Give the extent of all Plasmodium vivax-infected red blood cells.
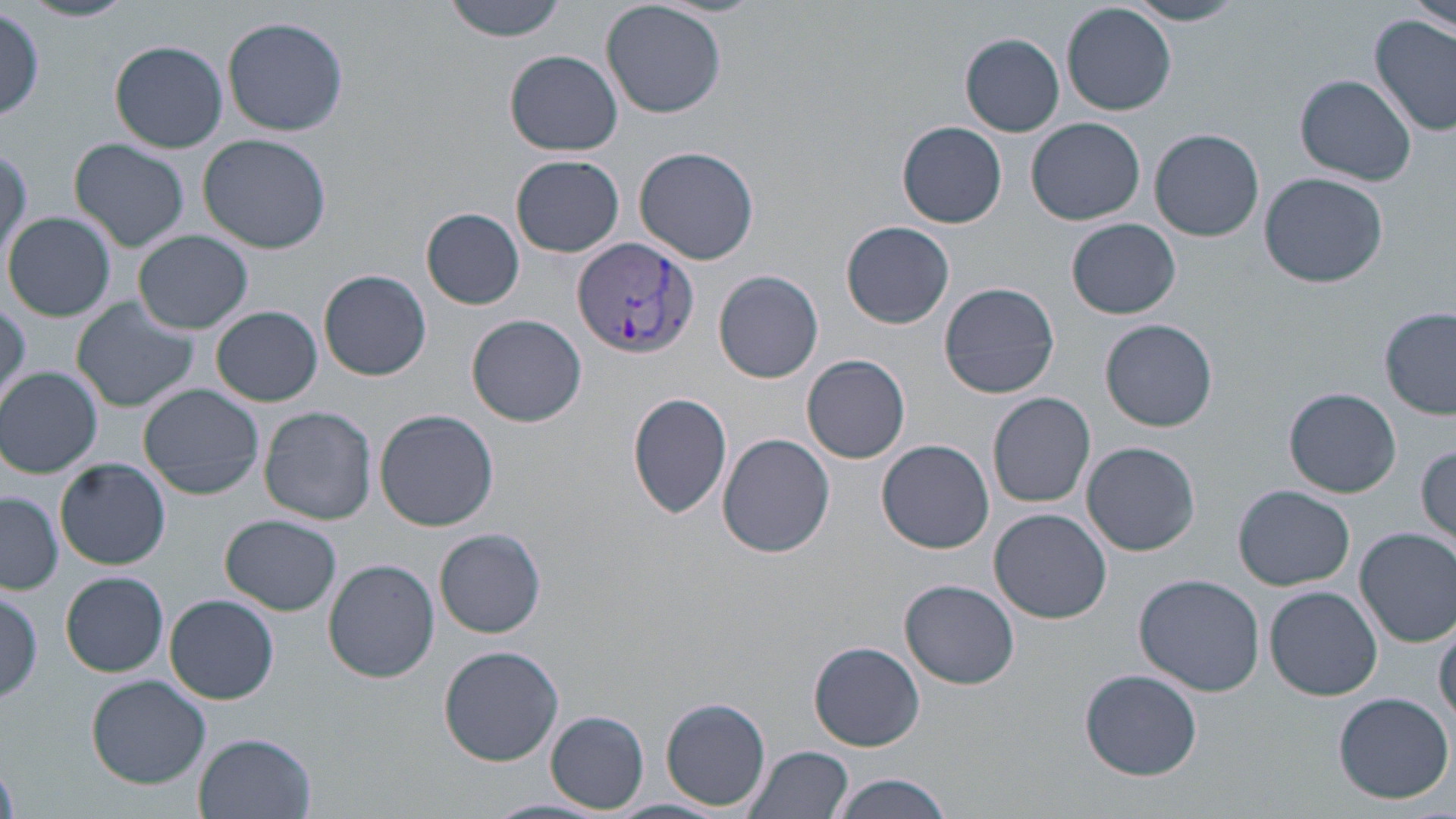

Approximate bounding boxes as named x1/y1/x2/y2 corners in pixels.
Plasmodium vivax-infected red blood cells: (x1=572, y1=236, x2=697, y2=359).

Uninfected red blood cell locations: (x1=23, y1=0, x2=136, y2=23), (x1=442, y1=0, x2=568, y2=42), (x1=603, y1=0, x2=729, y2=119), (x1=1410, y1=0, x2=1454, y2=35), (x1=1125, y1=1, x2=1247, y2=26), (x1=1062, y1=3, x2=1176, y2=115), (x1=1, y1=9, x2=46, y2=121), (x1=222, y1=16, x2=349, y2=136), (x1=1371, y1=17, x2=1456, y2=137), (x1=961, y1=34, x2=1063, y2=136), (x1=111, y1=40, x2=227, y2=152), (x1=506, y1=50, x2=622, y2=156), (x1=1294, y1=73, x2=1416, y2=185), (x1=1027, y1=117, x2=1145, y2=225), (x1=897, y1=122, x2=1007, y2=229), (x1=1149, y1=129, x2=1264, y2=242), (x1=197, y1=133, x2=332, y2=253), (x1=70, y1=138, x2=190, y2=252), (x1=635, y1=144, x2=761, y2=265), (x1=512, y1=155, x2=624, y2=257), (x1=1258, y1=172, x2=1388, y2=287), (x1=422, y1=207, x2=524, y2=309), (x1=5, y1=211, x2=115, y2=322), (x1=1068, y1=219, x2=1182, y2=320), (x1=842, y1=221, x2=954, y2=329), (x1=135, y1=230, x2=253, y2=334), (x1=319, y1=269, x2=432, y2=380), (x1=714, y1=270, x2=824, y2=383), (x1=939, y1=281, x2=1059, y2=398), (x1=74, y1=298, x2=202, y2=414), (x1=0, y1=302, x2=30, y2=402), (x1=211, y1=306, x2=322, y2=406), (x1=1381, y1=308, x2=1456, y2=419), (x1=467, y1=314, x2=587, y2=428), (x1=1101, y1=318, x2=1218, y2=431), (x1=802, y1=355, x2=911, y2=464), (x1=1, y1=365, x2=103, y2=477), (x1=138, y1=383, x2=263, y2=500), (x1=1283, y1=387, x2=1401, y2=498), (x1=628, y1=391, x2=733, y2=520), (x1=988, y1=392, x2=1096, y2=508), (x1=259, y1=406, x2=377, y2=525), (x1=374, y1=409, x2=500, y2=532), (x1=718, y1=433, x2=836, y2=558), (x1=878, y1=438, x2=995, y2=554), (x1=1080, y1=441, x2=1200, y2=556), (x1=1415, y1=443, x2=1455, y2=551), (x1=55, y1=458, x2=170, y2=570), (x1=1234, y1=485, x2=1355, y2=591), (x1=1, y1=491, x2=63, y2=594), (x1=990, y1=508, x2=1112, y2=623), (x1=222, y1=515, x2=342, y2=615), (x1=1354, y1=527, x2=1456, y2=646), (x1=435, y1=528, x2=546, y2=638), (x1=324, y1=559, x2=441, y2=683), (x1=61, y1=571, x2=169, y2=676), (x1=1133, y1=573, x2=1266, y2=696), (x1=900, y1=579, x2=1020, y2=689), (x1=1265, y1=586, x2=1382, y2=700), (x1=0, y1=589, x2=44, y2=703), (x1=165, y1=595, x2=279, y2=704), (x1=1434, y1=621, x2=1456, y2=727), (x1=809, y1=641, x2=925, y2=751), (x1=438, y1=644, x2=565, y2=767), (x1=1080, y1=668, x2=1203, y2=780), (x1=86, y1=675, x2=210, y2=788), (x1=1332, y1=691, x2=1455, y2=804), (x1=661, y1=698, x2=769, y2=810), (x1=547, y1=711, x2=649, y2=811), (x1=193, y1=733, x2=318, y2=819), (x1=742, y1=746, x2=853, y2=819), (x1=828, y1=774, x2=953, y2=819), (x1=484, y1=799, x2=606, y2=819). Slide-level diagnosis: Plasmodium vivax. Image is 1456×819 pixels. 1000x magnification. Light microscopy. Single field of view. May-Grünwald-Giemsa stain. Thin blood smear.